Identify the cell.
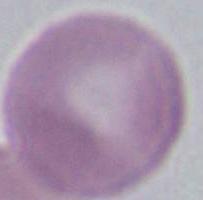

This is an erythrocyte.

1000x magnification. Photomicrograph.